Give the position of every malaria parasite.
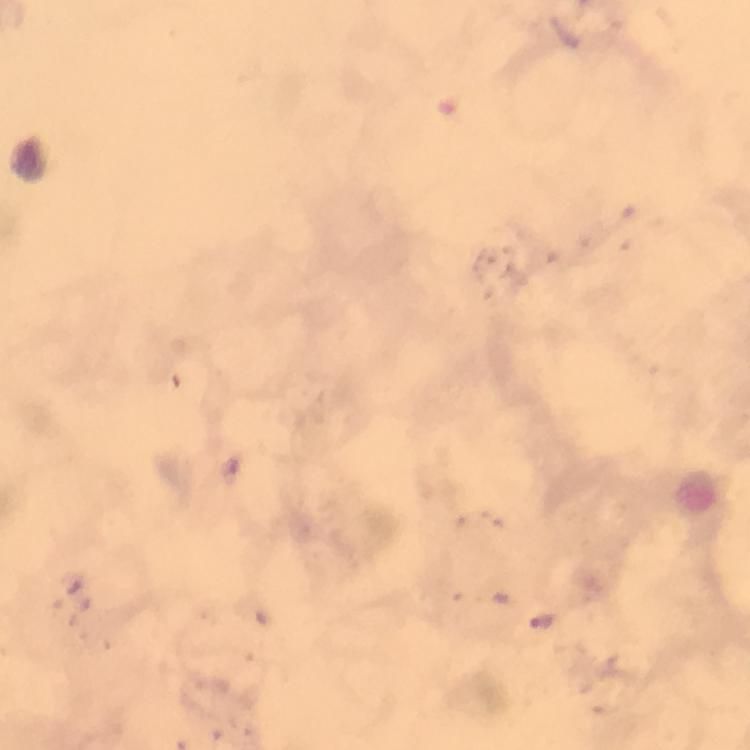

Approximate centers as (x, y) in pixels.
Malaria parasites: (543, 622).

stain: Giemsa
capture: smartphone photograph through a microscope
image_size: 750×750 pixels
preparation: thick smear
immersion_oil: applied
context: from a malaria diagnostic workup
cropped_from: one field of view
magnification: 100x